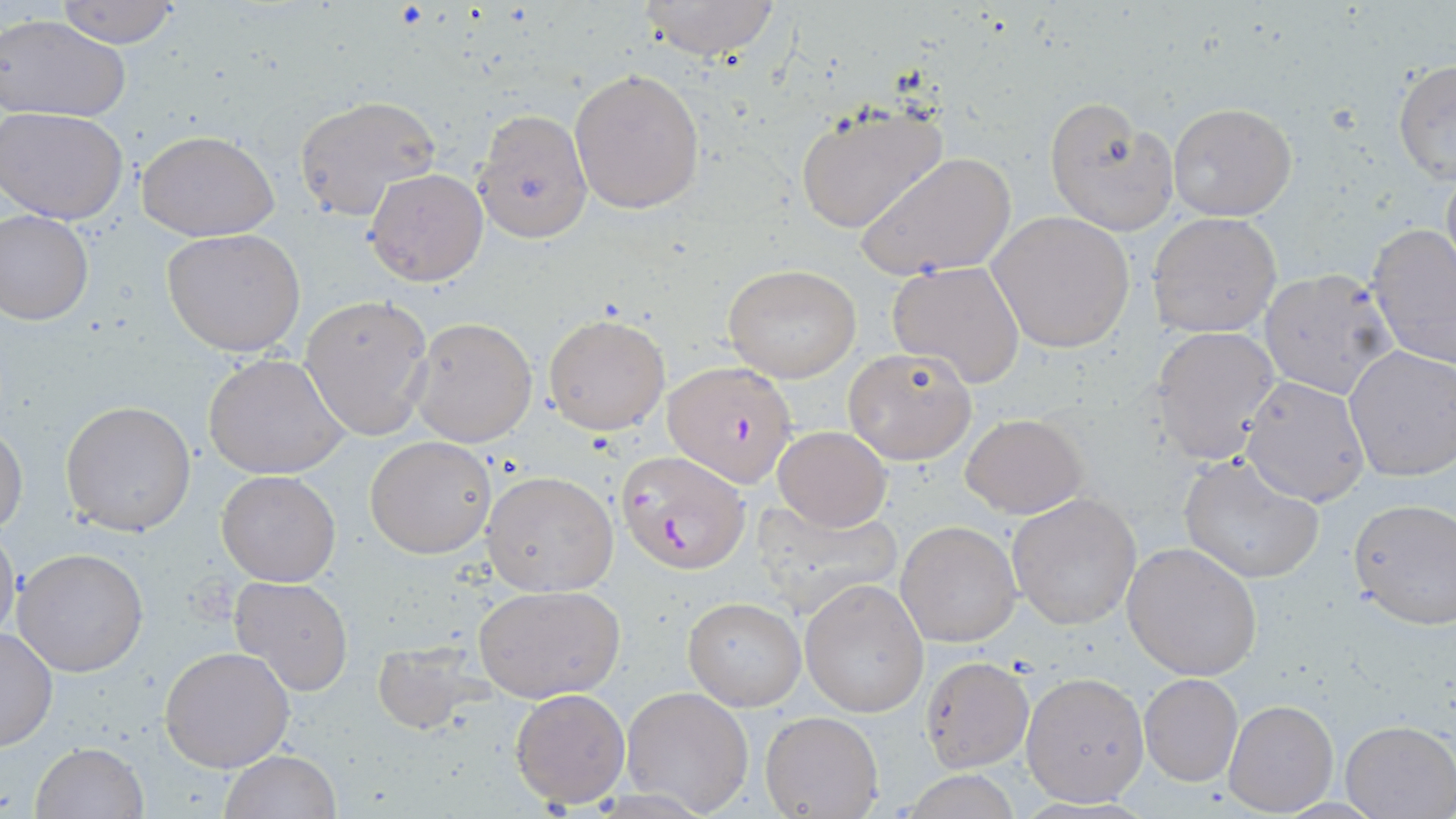
slide-level diagnosis = Plasmodium falciparum
modality = optical microscopy
Plasmodium falciparum-infected red blood cell locations = approximate bounding boxes as (x1, y1, x2, y2) in pixels: (664, 361, 800, 488), (614, 449, 748, 575)
stain = May-Grünwald-Giemsa
uninfected red blood cell locations = approximate bounding boxes as (x1, y1, x2, y2) in pixels: (51, 0, 189, 47), (634, 0, 782, 61), (0, 16, 132, 124), (1392, 59, 1456, 184), (569, 68, 707, 215), (293, 96, 439, 221), (1044, 98, 1176, 236), (1167, 100, 1297, 221), (792, 101, 949, 234), (2, 108, 129, 224), (472, 108, 593, 243), (137, 130, 280, 241), (858, 151, 1015, 283), (1440, 160, 1456, 283), (365, 168, 489, 286), (1, 209, 94, 325), (989, 210, 1136, 353), (1147, 211, 1282, 338), (1365, 223, 1456, 370), (163, 228, 306, 357), (887, 260, 1026, 387), (722, 264, 863, 383), (1258, 269, 1399, 400), (299, 293, 434, 441), (544, 313, 670, 435), (408, 315, 538, 448), (1151, 326, 1281, 464), (843, 346, 976, 465), (1342, 346, 1456, 483), (203, 353, 350, 480), (1240, 377, 1369, 506), (60, 400, 196, 536), (961, 413, 1087, 519), (1, 419, 28, 540), (772, 426, 892, 532), (366, 436, 496, 557), (1178, 455, 1324, 583), (216, 470, 341, 586), (482, 470, 619, 595), (1006, 492, 1142, 629), (747, 496, 903, 619), (1347, 498, 1456, 629), (0, 520, 22, 647), (895, 520, 1021, 648), (1122, 540, 1262, 681), (12, 547, 149, 677), (230, 574, 352, 697), (800, 578, 929, 718), (472, 583, 626, 704), (683, 597, 804, 711), (0, 627, 57, 751), (371, 638, 481, 732), (159, 644, 296, 772), (919, 655, 1033, 771), (1020, 672, 1149, 805), (1139, 674, 1242, 786), (620, 685, 755, 816), (509, 686, 632, 808), (1224, 699, 1337, 815), (760, 711, 884, 819), (1339, 720, 1454, 818), (29, 742, 147, 819), (221, 749, 340, 819)
field of view = one of a larger specimen
magnification = 1000x
image size = 1456×819 pixels
preparation = thin blood smear